Locate malaria parasites and leukocytes.
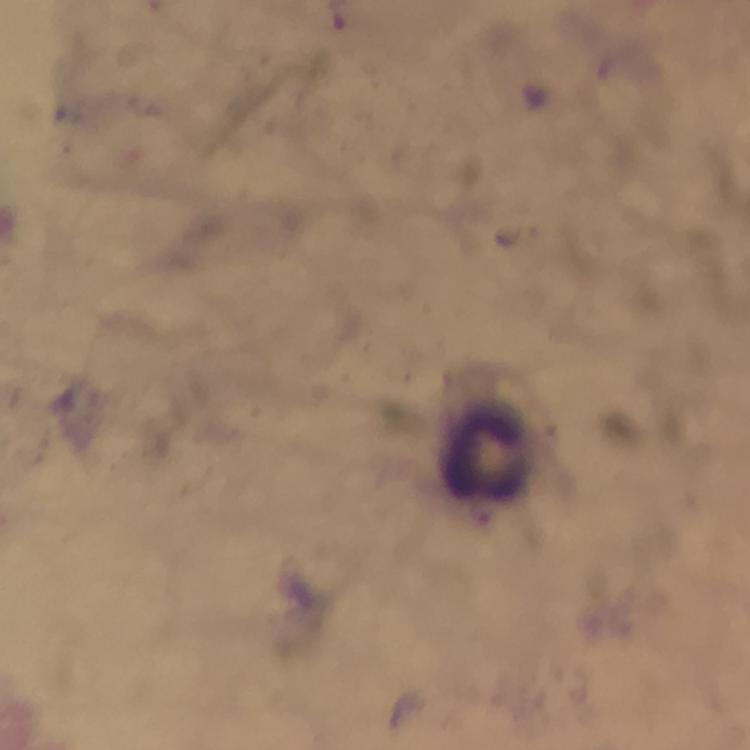

No malaria parasites seen.
Approximate centers as [x, y] in pixels.
Leukocytes: [483, 456].

magnification = 100x
immersion oil = used
image size = 750×750 pixels
stain = Giemsa
preparation = thick blood smear
context = from a malaria diagnostic workup
capture = smartphone photograph through a microscope
cropped from = a single field of view